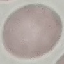 Result: no malaria parasites seen. Photographed with a smartphone camera at the microscope eyepiece. Giemsa stain. Thin blood smear. Automatically extracted cell patch, resized to 64 × 64 pixels.